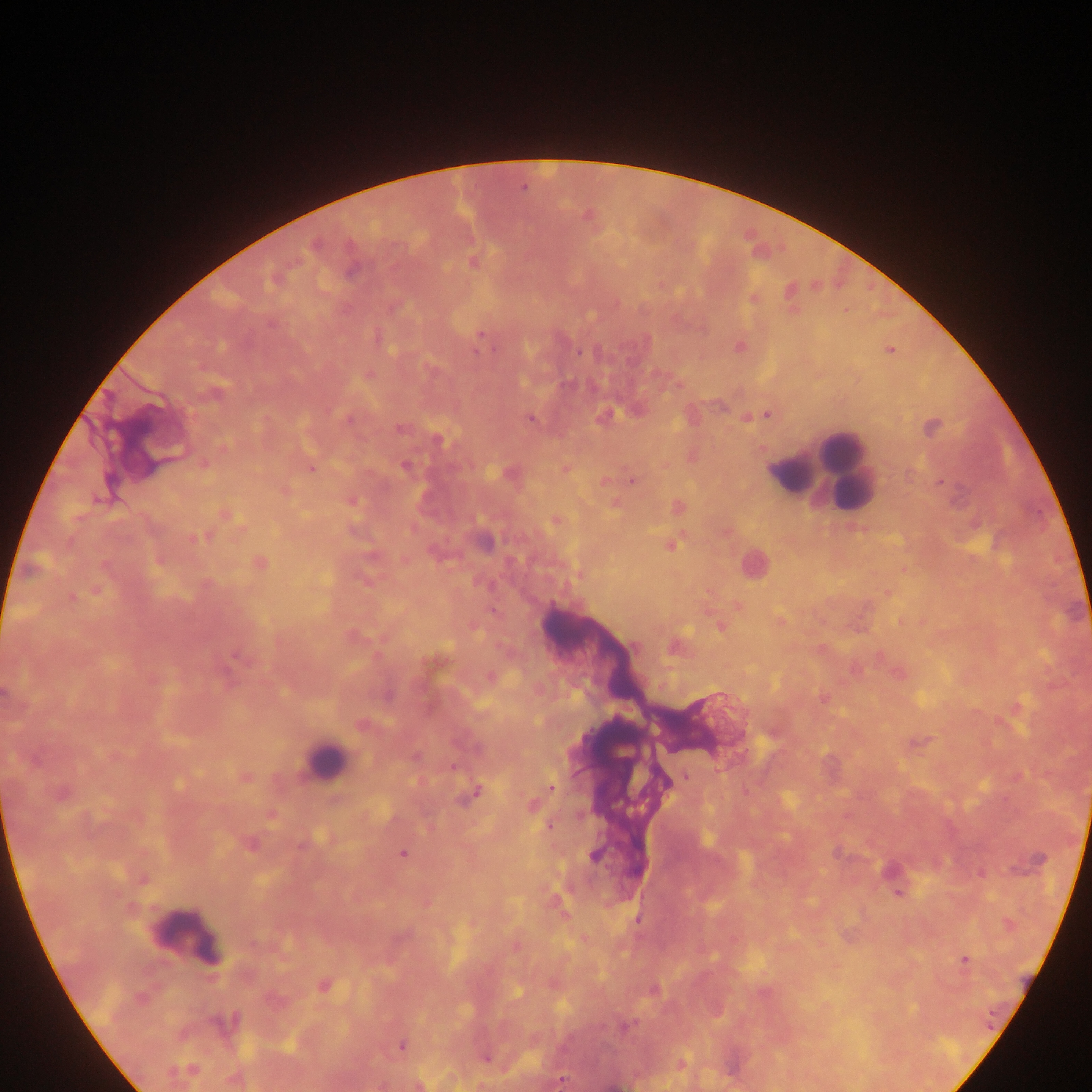
Approximate centers as (x, y) in pixels. Plasmodium parasite locations: (474, 263), (814, 288), (755, 297), (271, 322), (480, 333), (496, 347), (474, 349), (891, 350), (578, 352), (768, 414), (745, 417), (351, 418), (530, 418), (401, 429), (223, 447), (202, 463), (403, 466), (311, 468), (564, 468), (631, 480), (940, 482), (72, 597), (236, 654), (822, 695), (1017, 775), (247, 776), (684, 776), (551, 788), (531, 806), (271, 814), (550, 825), (402, 853), (981, 874), (898, 891), (965, 959), (324, 986). Leukocyte locations: (818, 469), (323, 763), (187, 937). Single field of view. Thick blood film. Collected in Ghana. Image is 1092×1092 pixels. Mobile-phone photograph taken through the microscope.